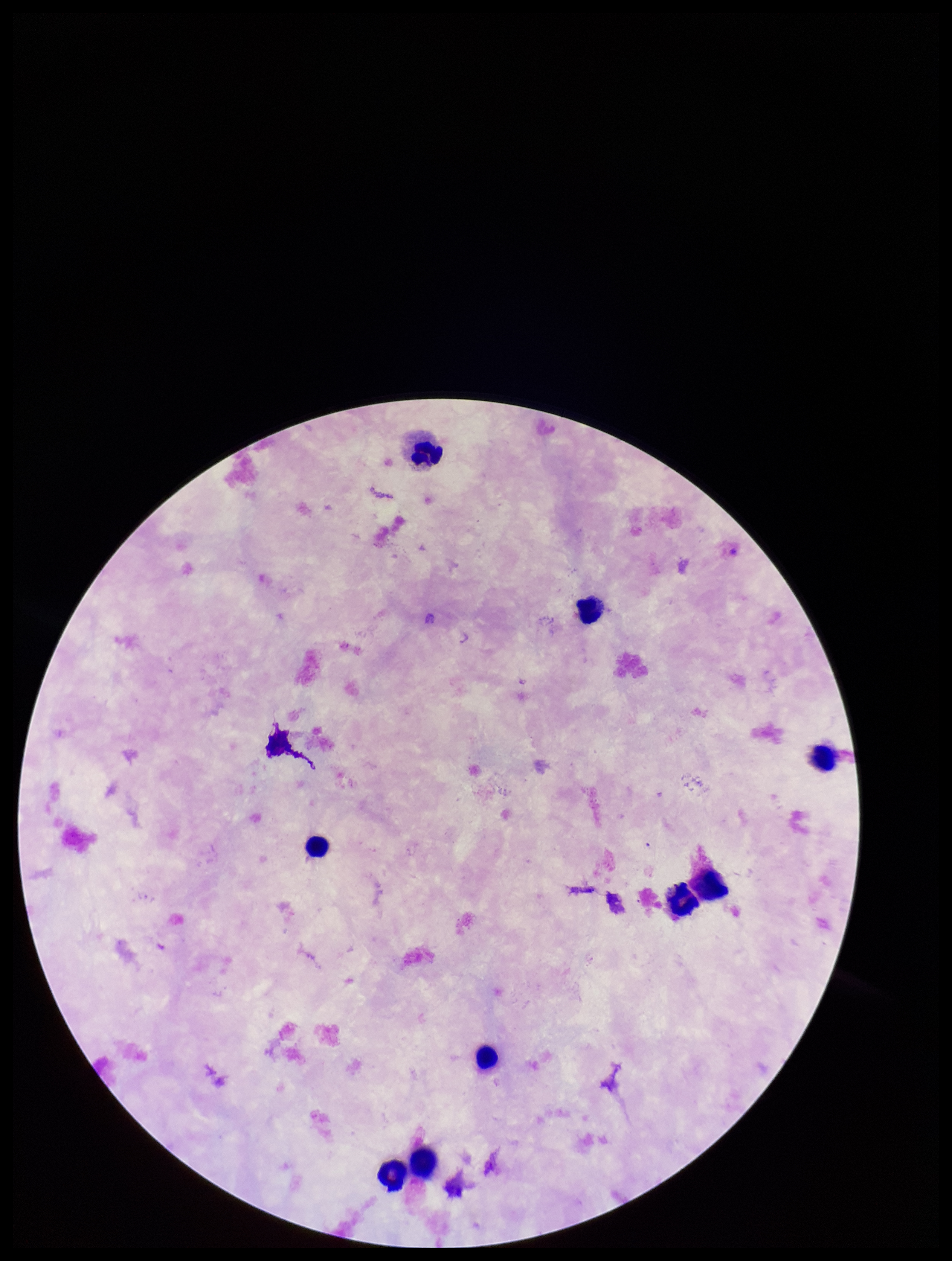

Summary:
  - Capture: smartphone photograph through the microscope eyepiece
  - Parasite count: 0
  - Image size: 952×1261 pixels
  - Plasmodium parasites: none detected
  - Patient malaria status: negative
  - Leukocyte count: 9
  - Preparation: thick blood smear
  - Stain: Giemsa
  - Field of view: single